Give a bounding box for every leukocyte visible.
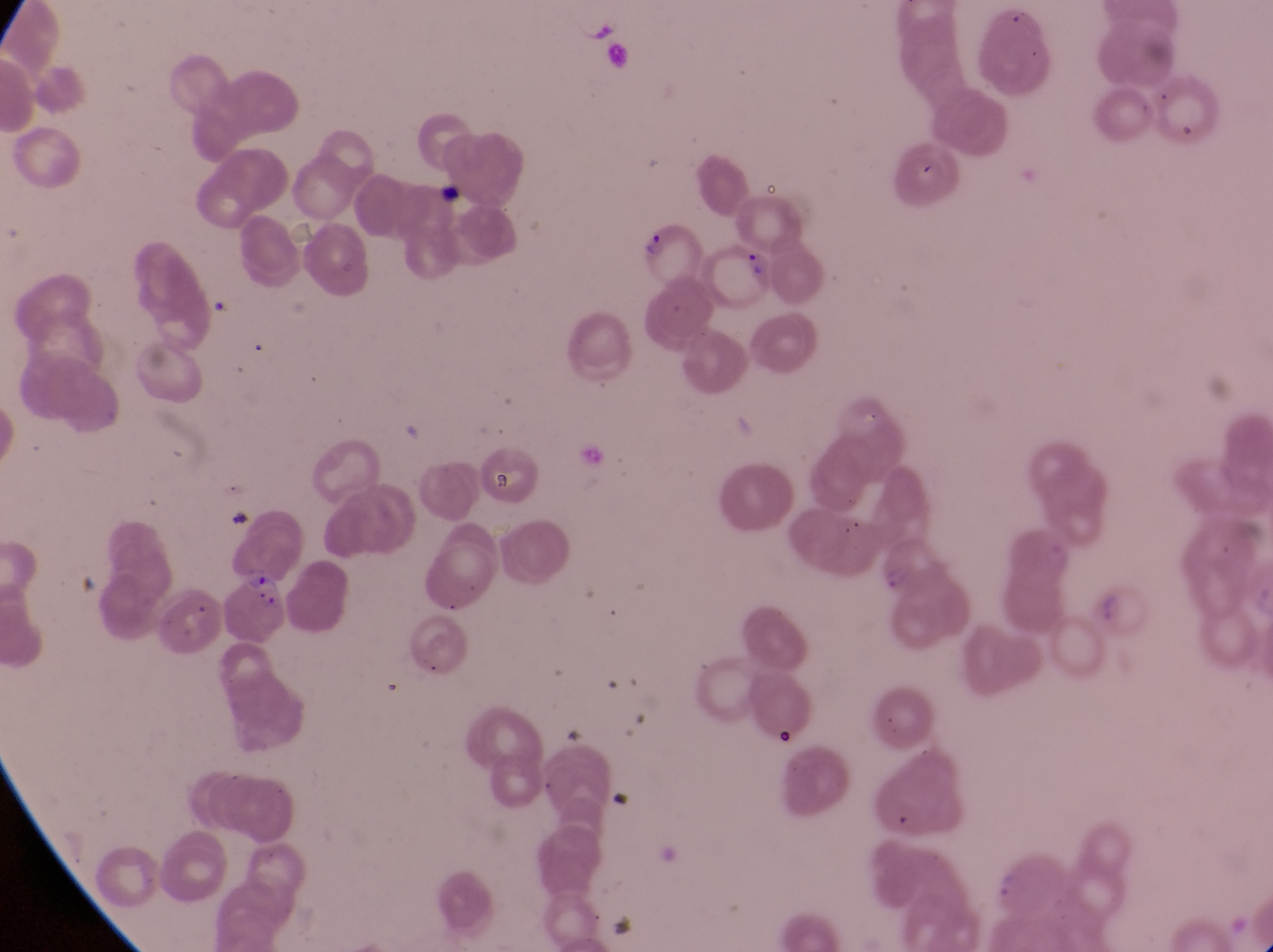
No leukocytes observed.

Approximate bounding boxes as left top right bottom in pixels. Parasitised red blood cell locations: 636 220 699 287; 706 240 773 305; 880 540 942 597; 230 563 290 636. Artifact (platelet-like body, stain precipitate, or debris) locations: 484 454 534 509. Captured by a smartphone held over the eyepiece of an Olympus CX-23 microscope. Collected in Uganda. Image is 1273×952 pixels. Magnification of 1000x. Thin blood film. Single field of view.